Report the malaria status of this cell.
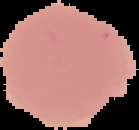

Uninfected.

{
  "image_size": "139×130 pixels",
  "image_type": "segmented cell region on a black background",
  "preparation": "thin blood smear"
}